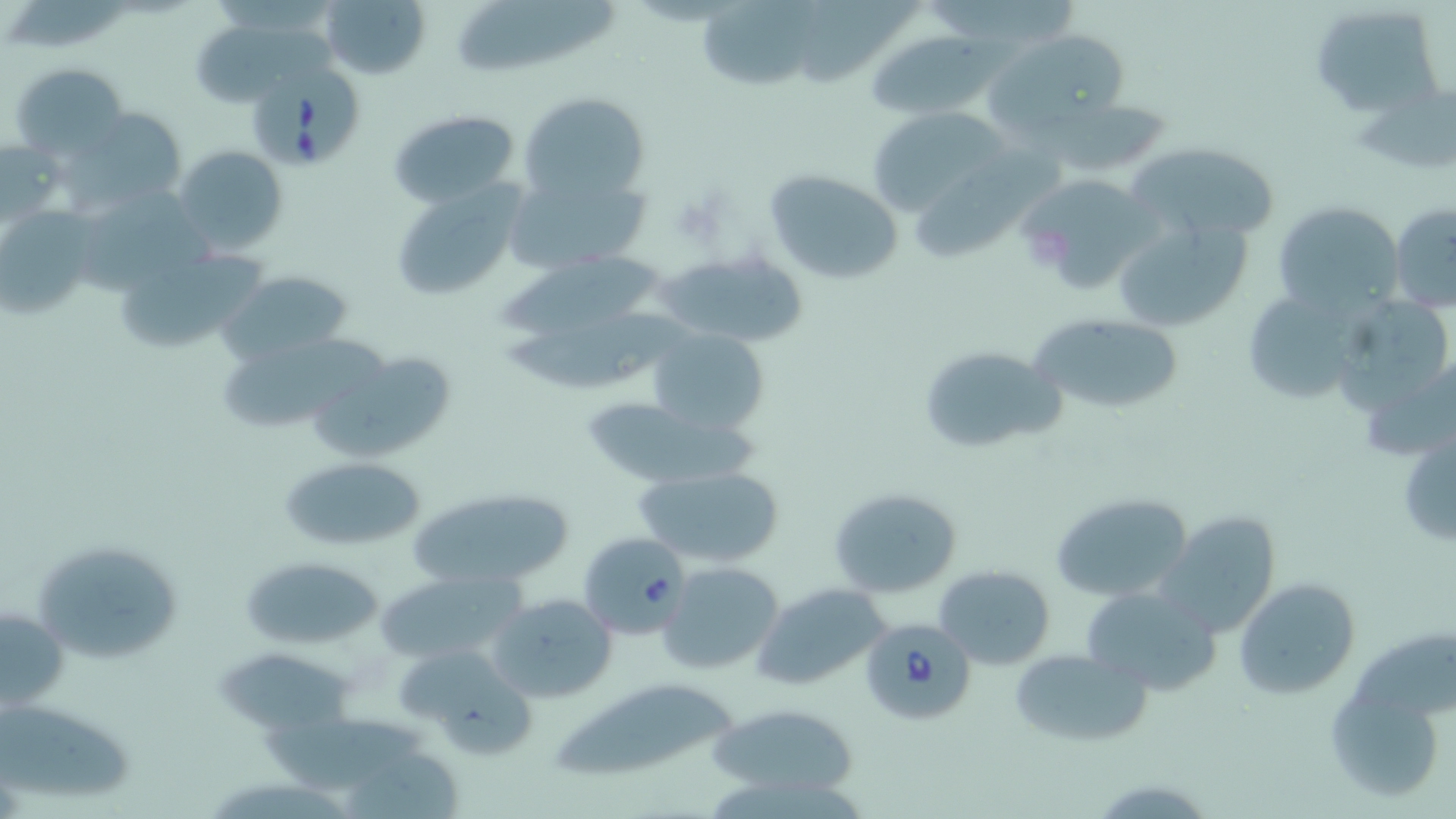 Approximate bounding boxes as (x1, y1, x2, y2) in pixels. Babesia divergens-infected red blood cell locations: (244, 60, 361, 172), (579, 530, 691, 639), (858, 616, 976, 724). Uninfected red blood cell locations: (321, 0, 431, 82), (449, 2, 629, 75), (1306, 5, 1441, 117), (193, 21, 340, 101), (985, 29, 1135, 139), (868, 32, 991, 120), (9, 62, 129, 161), (519, 91, 650, 205), (1037, 99, 1173, 176), (865, 105, 1011, 216), (75, 107, 187, 208), (388, 109, 521, 206), (912, 131, 1060, 265), (1, 138, 66, 230), (1127, 142, 1282, 244), (174, 143, 289, 256), (505, 168, 649, 274), (763, 168, 906, 286), (1015, 174, 1156, 294), (387, 179, 527, 303), (1270, 200, 1402, 316), (1389, 202, 1456, 313), (0, 208, 95, 319), (1108, 213, 1253, 335), (113, 247, 266, 356), (652, 247, 814, 348), (487, 252, 667, 334), (217, 271, 353, 363), (1239, 287, 1370, 406), (1334, 289, 1445, 421), (503, 307, 691, 396), (1031, 315, 1185, 413), (648, 328, 769, 436), (916, 344, 1063, 456), (313, 350, 463, 465), (576, 398, 756, 489), (1397, 426, 1456, 551), (279, 454, 424, 552), (634, 465, 785, 567), (406, 486, 575, 591), (829, 487, 962, 597), (1049, 492, 1193, 602), (1156, 511, 1287, 635), (31, 536, 187, 665), (242, 555, 385, 651), (657, 561, 784, 675), (933, 562, 1056, 669), (374, 570, 522, 664), (1235, 578, 1360, 701), (750, 582, 894, 694), (1081, 583, 1218, 695), (486, 593, 617, 703), (1, 601, 69, 714), (393, 642, 538, 757), (1010, 648, 1147, 743), (216, 651, 354, 730), (548, 677, 740, 782), (1326, 691, 1444, 801), (1, 698, 137, 802), (707, 703, 860, 800), (254, 716, 438, 786). Slide-level diagnosis: Babesia divergens. Thin blood film. Light microscopy. May-Grünwald-Giemsa stain. Image is 1456×819 pixels. One field of a larger specimen. 1000x magnification.